Describe the morphology of the red blood cells.
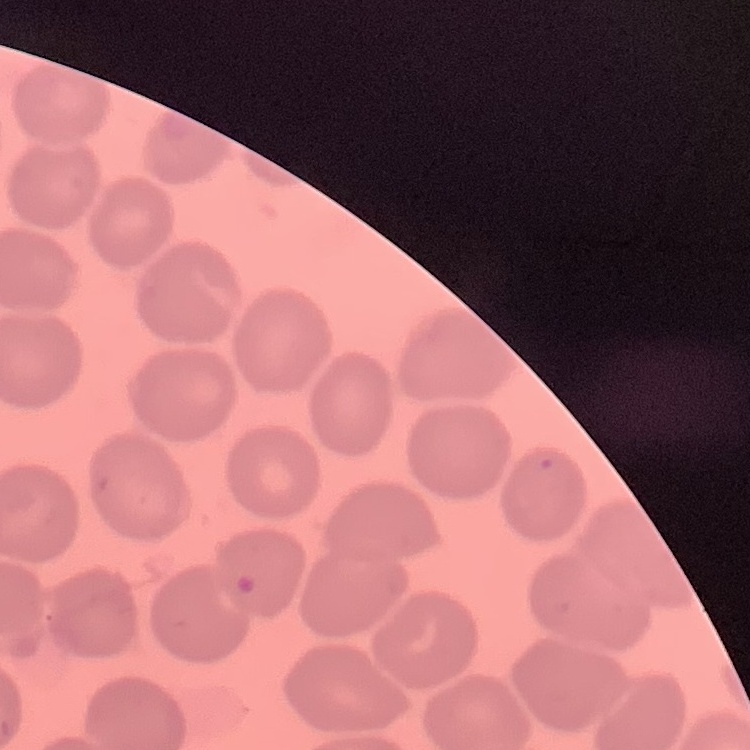
No rouleaux formation.

image type = square crop of a larger photomicrograph
stain = Field's or Giemsa
preparation = thin blood film